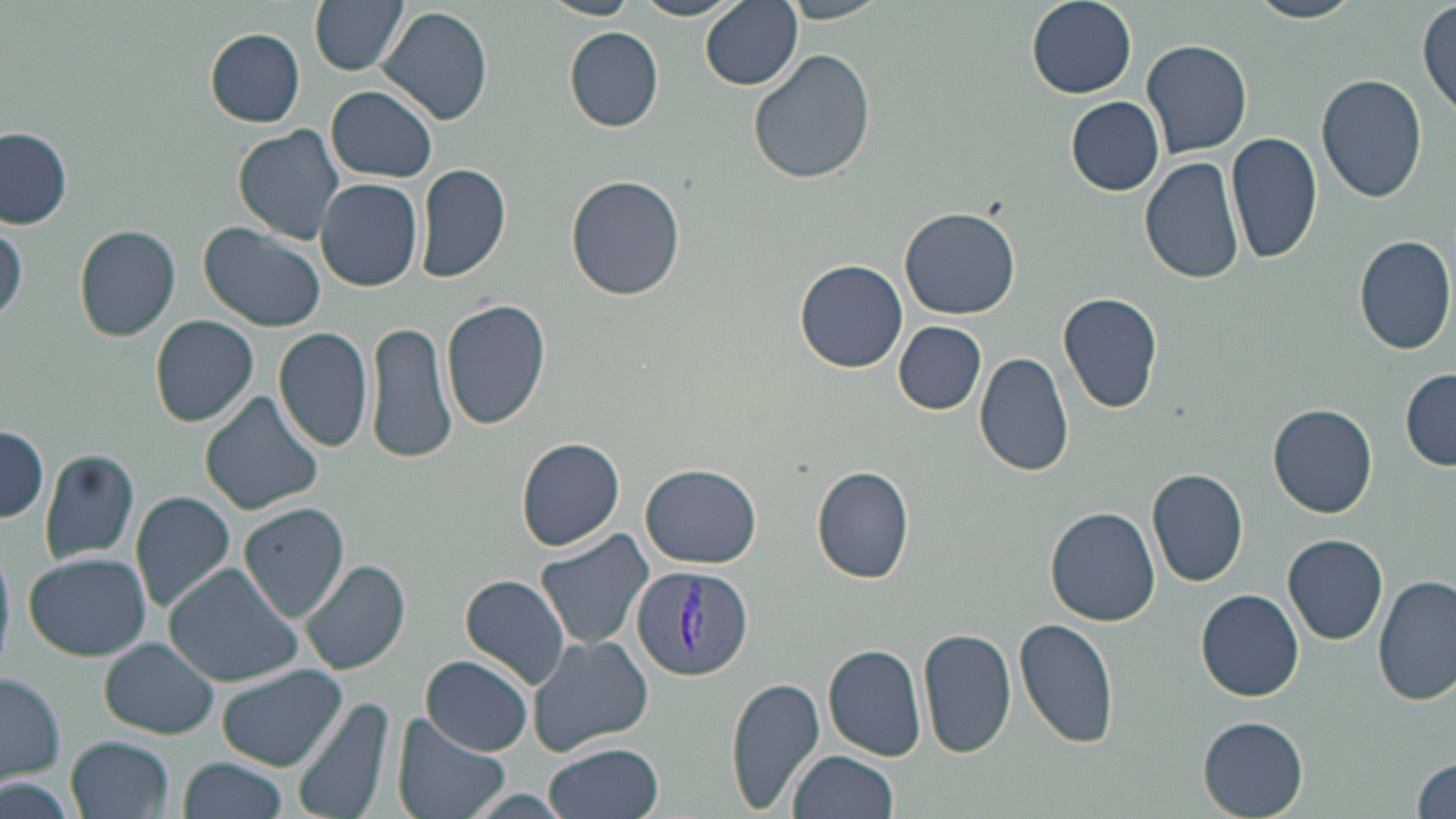
Approximate bounding boxes as [x1, y1, x2, y2] in pixels. Plasmodium vivax-infected red blood cell locations: [629, 564, 753, 683]. Uninfected red blood cell locations: [309, 0, 408, 76], [542, 0, 637, 20], [629, 0, 744, 20], [1027, 0, 1137, 97], [1245, 0, 1366, 24], [702, 1, 803, 91], [773, 1, 895, 22], [1417, 2, 1454, 116], [377, 6, 493, 125], [205, 28, 306, 126], [566, 28, 663, 131], [1141, 37, 1253, 158], [748, 49, 876, 185], [1317, 73, 1429, 204], [328, 86, 437, 183], [1066, 97, 1164, 195], [234, 124, 346, 245], [0, 127, 73, 228], [1226, 129, 1320, 266], [1140, 154, 1246, 285], [415, 163, 512, 285], [566, 174, 685, 301], [316, 178, 424, 292], [900, 207, 1020, 319], [0, 217, 27, 328], [199, 219, 330, 332], [75, 225, 181, 341], [1354, 233, 1455, 355], [795, 259, 908, 374], [1059, 291, 1164, 414], [442, 298, 551, 431], [150, 315, 260, 428], [367, 319, 460, 466], [894, 322, 986, 414], [274, 326, 375, 452], [974, 349, 1077, 479], [1401, 370, 1456, 469], [201, 392, 323, 517], [1268, 403, 1379, 518], [0, 425, 49, 524], [517, 437, 624, 550], [38, 447, 141, 565], [639, 463, 762, 568], [812, 466, 915, 584], [1147, 467, 1249, 587], [131, 490, 236, 613], [239, 502, 350, 623], [1046, 506, 1162, 625], [536, 527, 655, 652], [1283, 534, 1389, 645], [471, 548, 646, 677], [23, 552, 151, 661], [299, 558, 410, 677], [162, 563, 304, 685], [460, 573, 572, 690], [1373, 573, 1455, 705], [1196, 588, 1304, 702], [1013, 618, 1119, 753], [919, 627, 1016, 760], [528, 633, 653, 753], [101, 641, 218, 735], [824, 641, 930, 761], [422, 655, 534, 756], [214, 664, 348, 774], [1, 670, 67, 782], [726, 677, 826, 812], [291, 693, 400, 819], [393, 712, 513, 819], [1197, 716, 1309, 819], [67, 735, 171, 817], [545, 743, 664, 819], [787, 750, 898, 819], [1410, 753, 1456, 819], [180, 756, 287, 819], [2, 774, 84, 819], [454, 788, 583, 819]. Slide-level diagnosis: Plasmodium vivax. One field of a larger specimen. Captured at 1000x magnification. Image is 1456×819 pixels. Thin blood film. May-Grünwald-Giemsa stain. Light microscopy.